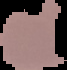
{
  "image_size": "67×70 pixels",
  "preparation": "thin blood film",
  "malaria_status": "parasitized",
  "image_type": "cell region segmented out of the field of view; surrounding area masked to black"
}